Point out each Plasmodium parasite and each leukocyte.
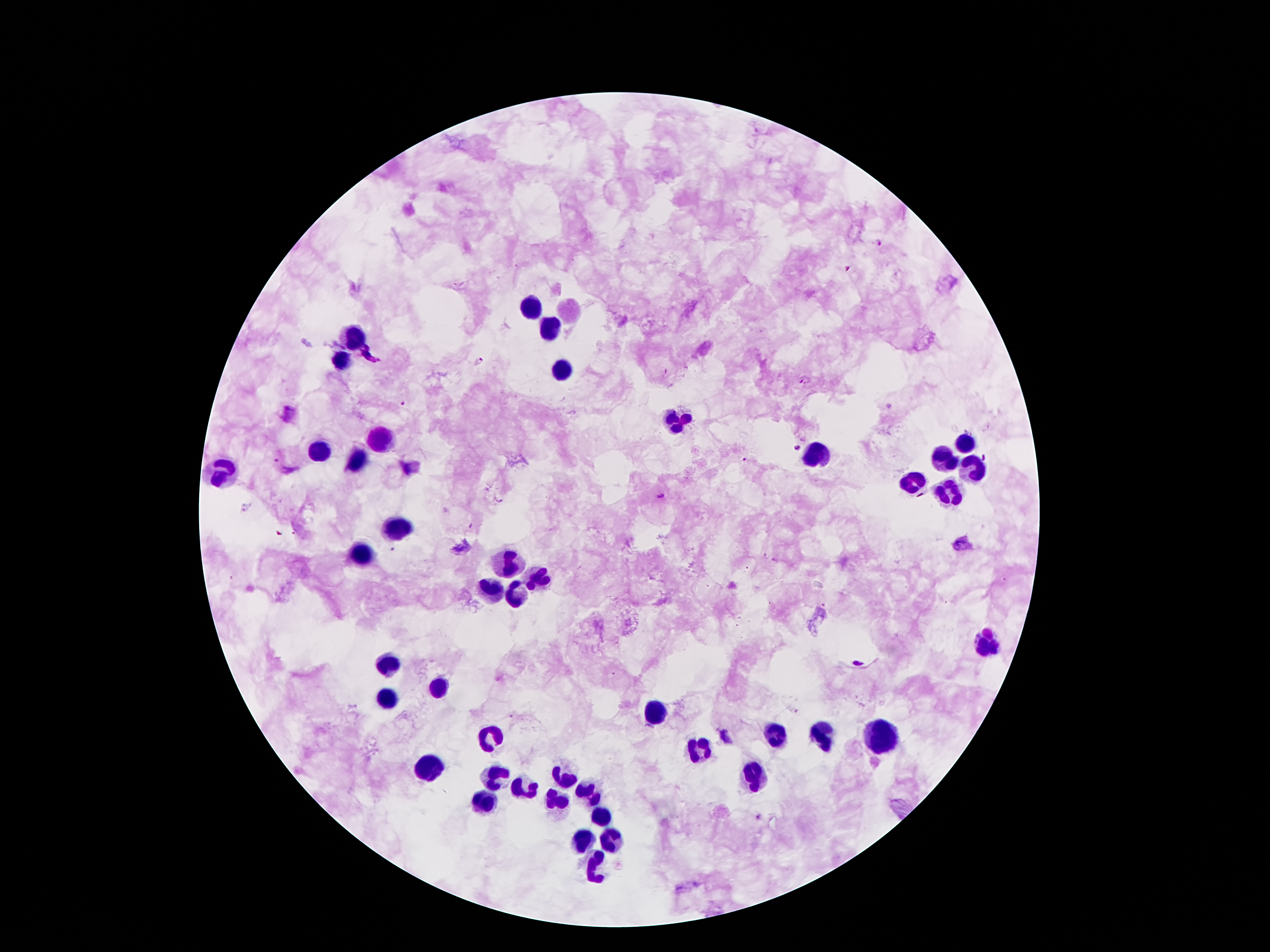
Approximate centers as (x, y) in pixels.
Plasmodium parasites: (879, 242), (848, 267), (480, 359), (806, 380), (403, 400), (795, 446), (744, 459), (273, 460), (660, 496), (246, 506), (469, 525), (391, 549), (858, 663), (758, 817).
Leukocytes: (531, 306), (547, 327), (354, 335), (342, 360), (562, 369), (676, 420), (381, 438), (966, 445), (317, 449), (819, 454), (944, 458), (354, 460), (969, 470), (222, 472), (914, 483), (948, 490), (396, 527), (362, 551), (508, 565), (535, 579), (488, 590), (517, 595), (985, 645), (387, 663), (440, 692), (385, 699), (658, 711), (821, 736), (490, 738), (778, 738), (883, 740), (703, 751), (431, 767), (496, 778), (753, 778), (563, 781), (524, 788), (585, 790), (560, 801), (483, 803), (601, 815), (610, 838), (583, 842), (594, 869).

Thick peripheral-blood smear. Smartphone photograph taken through the microscope eyepiece. 100x magnification. Giemsa stain. Image is 1270×952 pixels. Patient malaria status: positive for Plasmodium falciparum. One field from this slide.